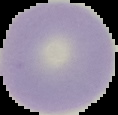

From a thin blood smear. Segmented cell region on a black background. Image is 118×115 pixels. Malaria status: uninfected.